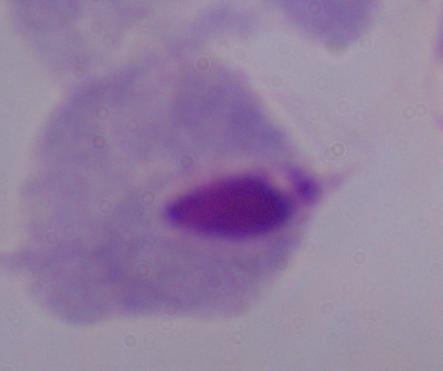
Captured at 1000x magnification. Photomicrograph. A trichomonad is seen.